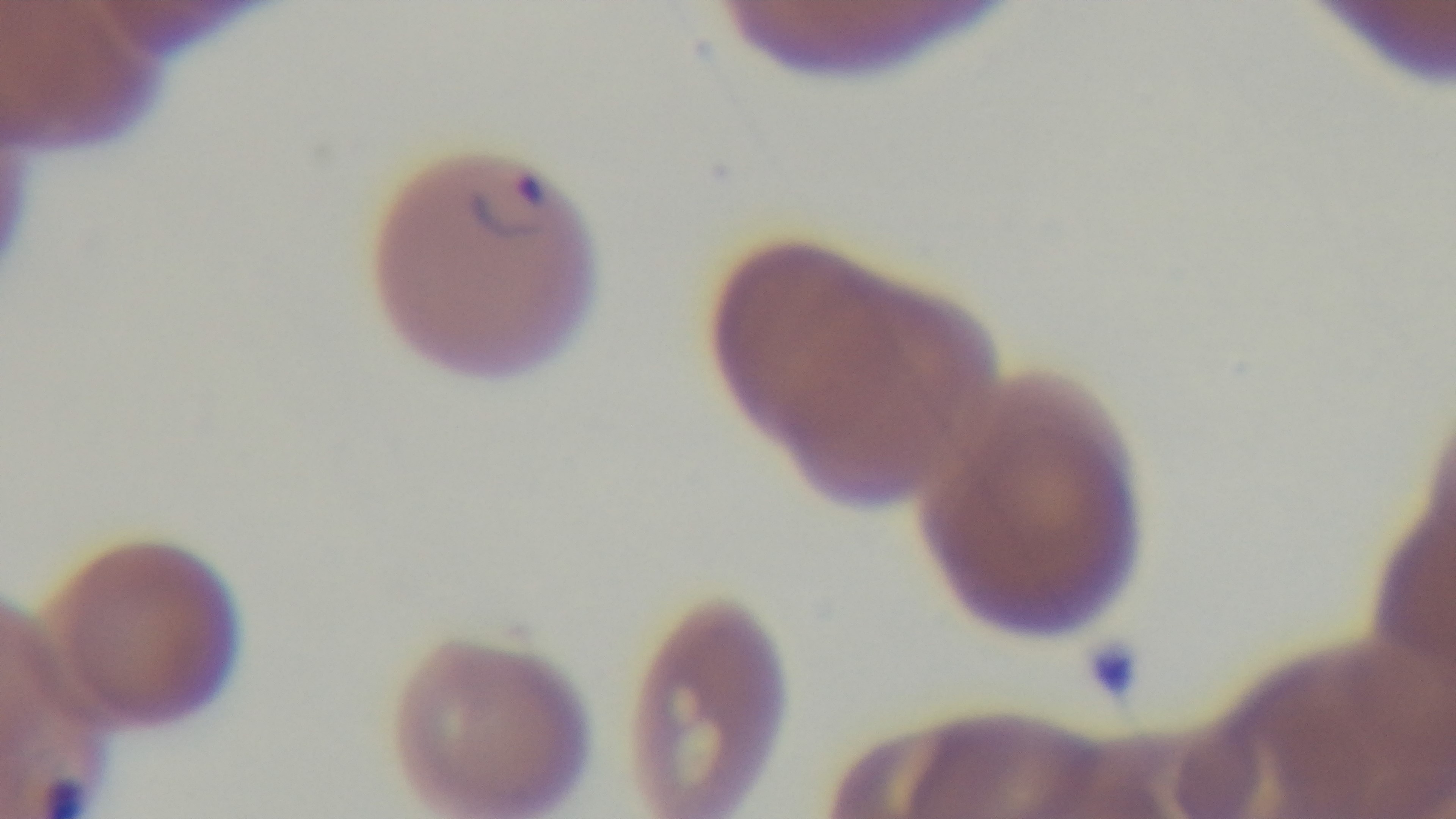

{
  "field_of_view": "one from the slide",
  "modality": "light microscopy",
  "malaria_status": "positive",
  "capture": "mounted 4K digital camera",
  "objective": "100x oil immersion",
  "preparation": "thin blood film",
  "stain": "Giemsa"
}